Assess the morphology of the erythrocytes.
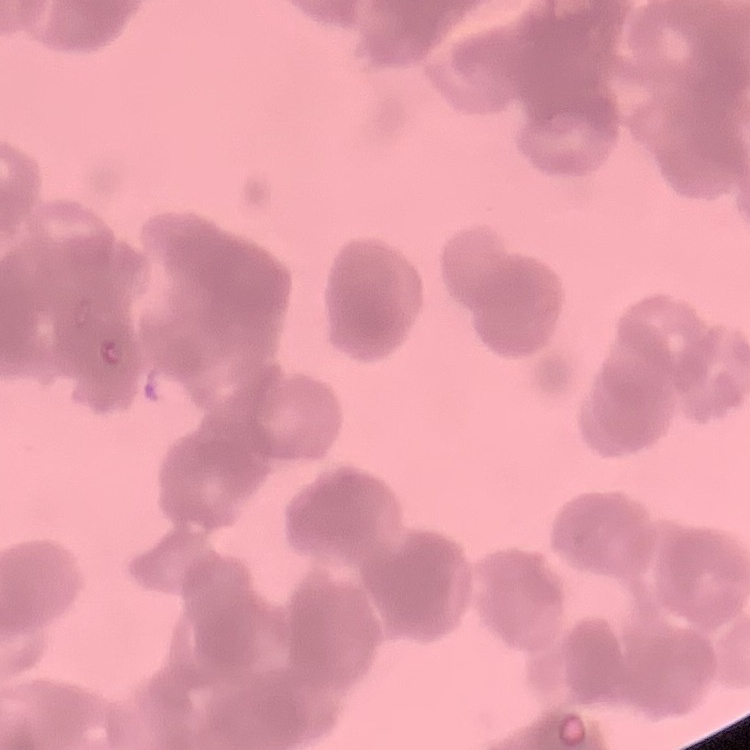

Rouleaux formation.

Summary:
  - Stain: Field's or Giemsa
  - Image type: square crop of a larger photomicrograph
  - Preparation: thin peripheral smear